Report the malaria status of this cell.
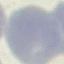
It is uninfected.

Summary:
  - Preparation: thin blood smear
  - Image type: automatically extracted cell patch, resized to 64 × 64 pixels
  - Capture: smartphone through the microscope eyepiece
  - Stain: Giemsa